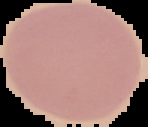

Summary:
  - Image size: 148×127 pixels
  - Image type: segmented cell region on a black background
  - Result: negative for Plasmodium parasites
  - Preparation: thin blood film